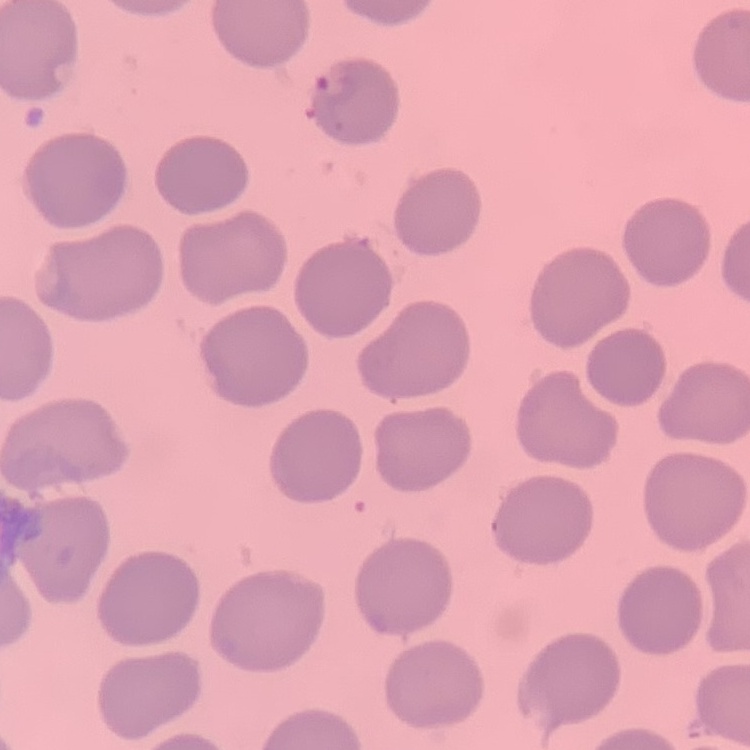 The red blood cells exhibit no rouleaux formation. One tile cut from a larger photomicrograph. Thin peripheral smear. Stained with either Field's or Giemsa.